Assess this cell for malaria.
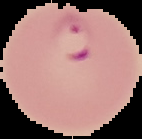
It is parasitized.

Summary:
  - Image size: 142×139 pixels
  - Image type: segmented cell region on a black background
  - Preparation: thin blood smear